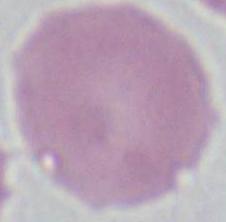

modality = micrograph
identification = erythrocyte
magnification = 1000x